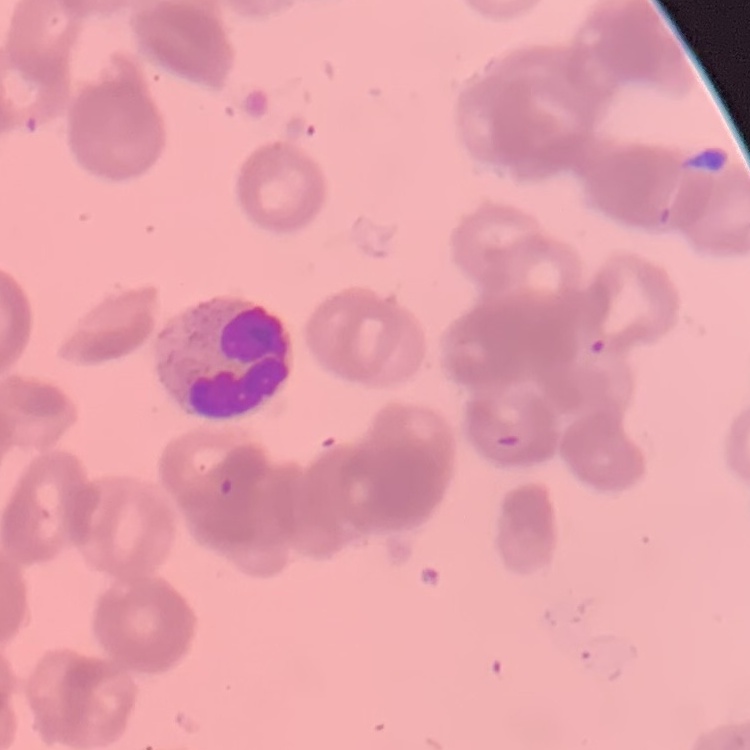

Summary:
  - Red blood cell morphology: rouleaux formation
  - Image type: square crop of a larger photomicrograph
  - Preparation: thin blood film
  - Stain: Field's or Giemsa